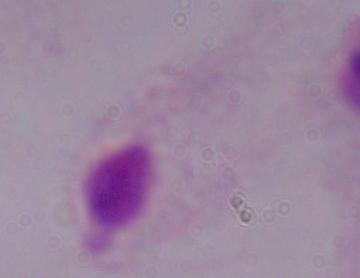

Photomicrograph. A trichomonad is shown. Captured at 1000x magnification.